State which parasite is depicted.
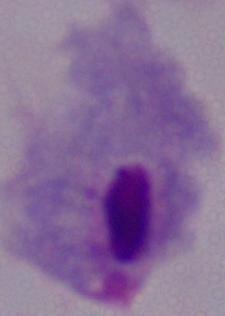

This is a trichomonad.

Summary:
  - Magnification: 1000x
  - Modality: micrograph